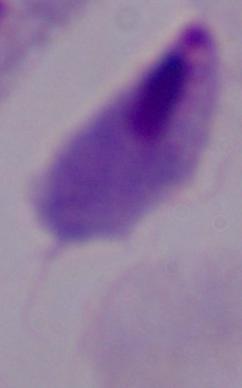

Micrograph. A trichomonad is seen. 1000x magnification.